Give the preparation type.
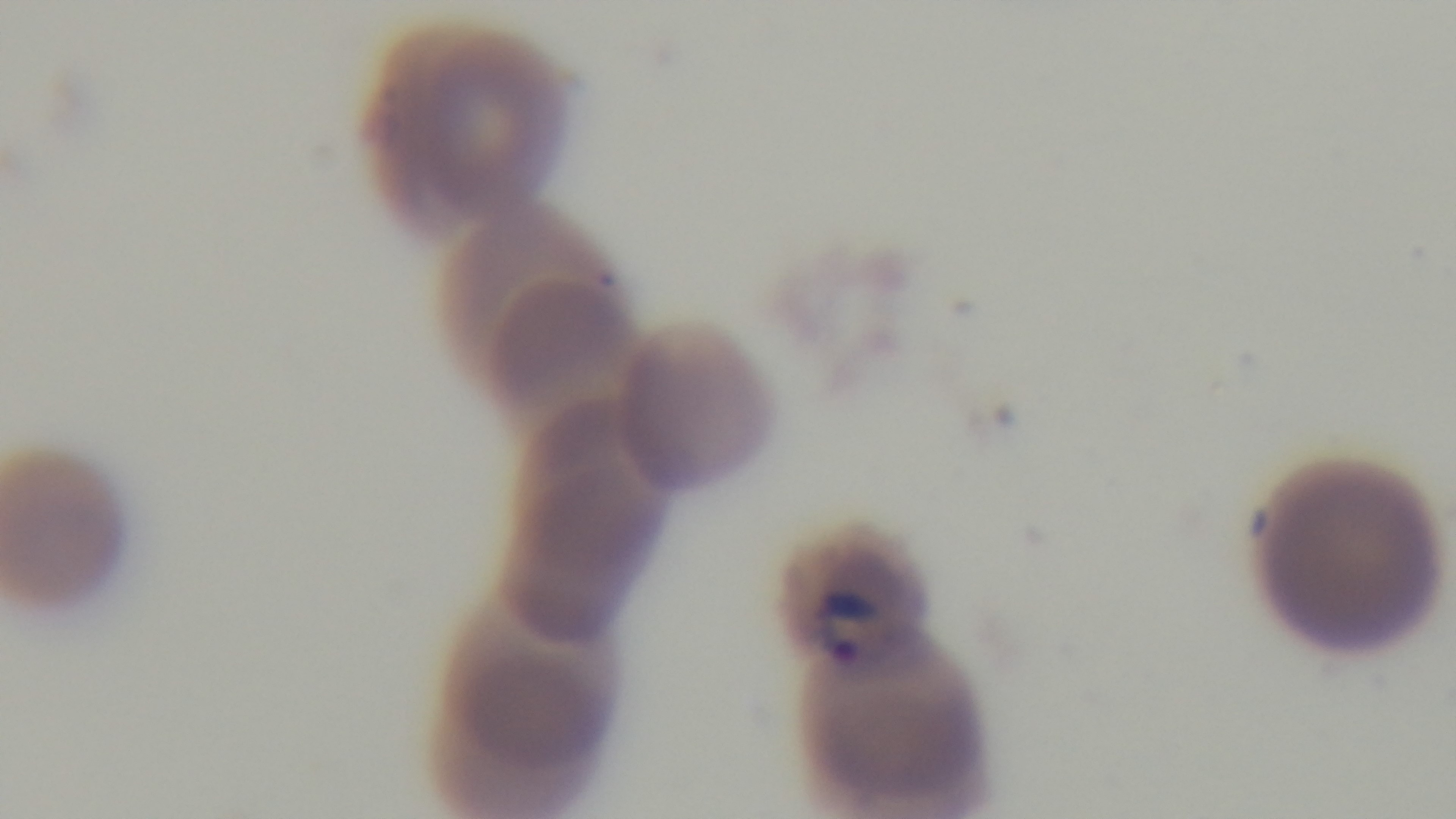
A thin smear.

malaria status = infected
objective = 100x oil immersion
field of view = single
stain = Giemsa
capture = mounted 4K digital camera
modality = light microscopy